Describe the morphology of the erythrocytes.
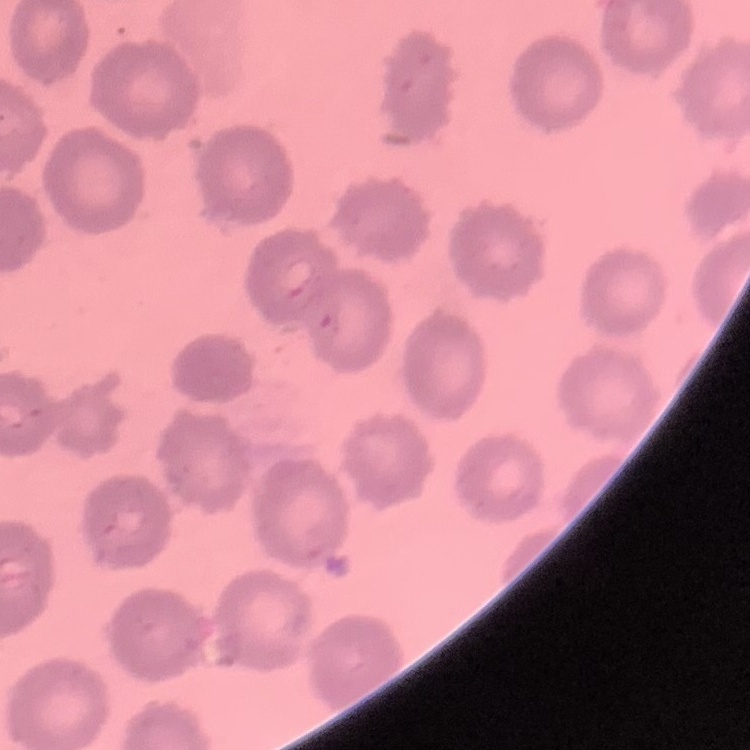

They show no rouleaux formation.

Thin blood film. Field's or Giemsa stain. Square crop of a larger photomicrograph.